Classify this cell by malaria status.
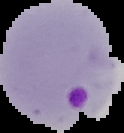

Parasitized.

Summary:
  - Image type: segmented cell region with the area outside set to black
  - Preparation: thin blood film
  - Image size: 124×133 pixels